Assess the morphology of the erythrocytes.
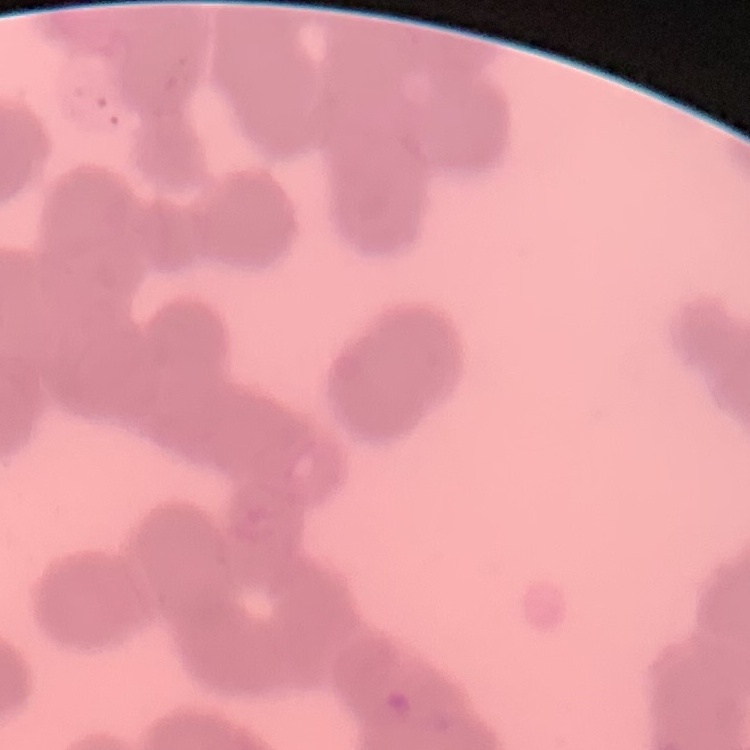

They show rouleaux formation.

Thin blood smear. Square crop of a larger photomicrograph. Stained with either Field's or Giemsa.